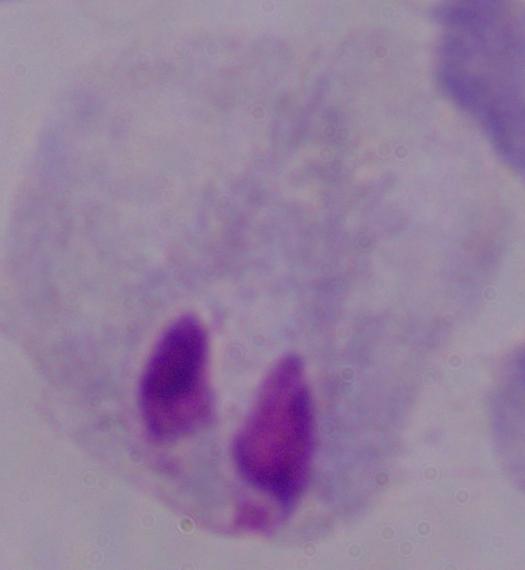
modality = micrograph
identification = trichomonad
magnification = 1000x